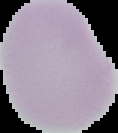
Summary:
  - Preparation: thin blood film
  - Image size: 118×133 pixels
  - Malaria status: uninfected
  - Image type: segmented cell region on a black background